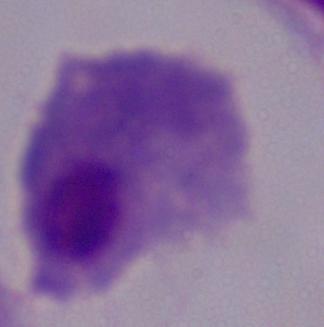
Summary:
  - Identification: trichomonad
  - Magnification: 1000x
  - Modality: micrograph